Assess this cell for malaria.
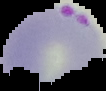

It is parasitized.

Summary:
  - Image size: 106×91 pixels
  - Preparation: thin blood smear
  - Image type: segmented cell region with the area outside set to black